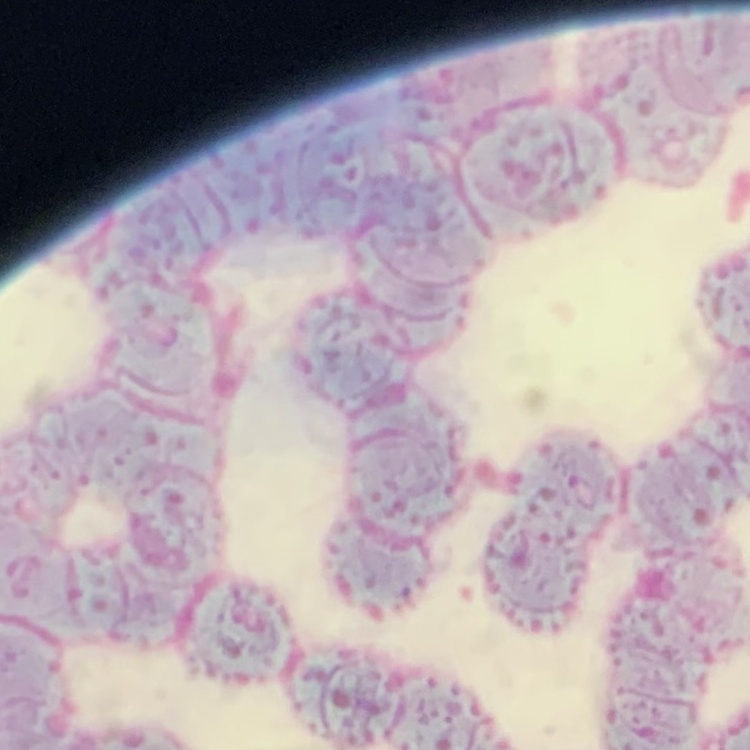

Summary:
  - Red blood cell morphology: rouleaux formation
  - Stain: Field's or Giemsa
  - Preparation: thin peripheral smear
  - Image type: square crop of a larger photomicrograph